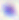

Summary:
  - Modality: photomicrograph
  - Identification: Toxoplasma gondii
  - Magnification: 400x